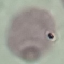

Summary:
  - Malaria status: uninfected
  - Capture: smartphone through the microscope eyepiece
  - Preparation: thin blood film
  - Stain: Giemsa
  - Image type: cell patch, automatically extracted from a larger field of view and resized to 64 × 64 pixels